Locate every leukocyte (white blood cell).
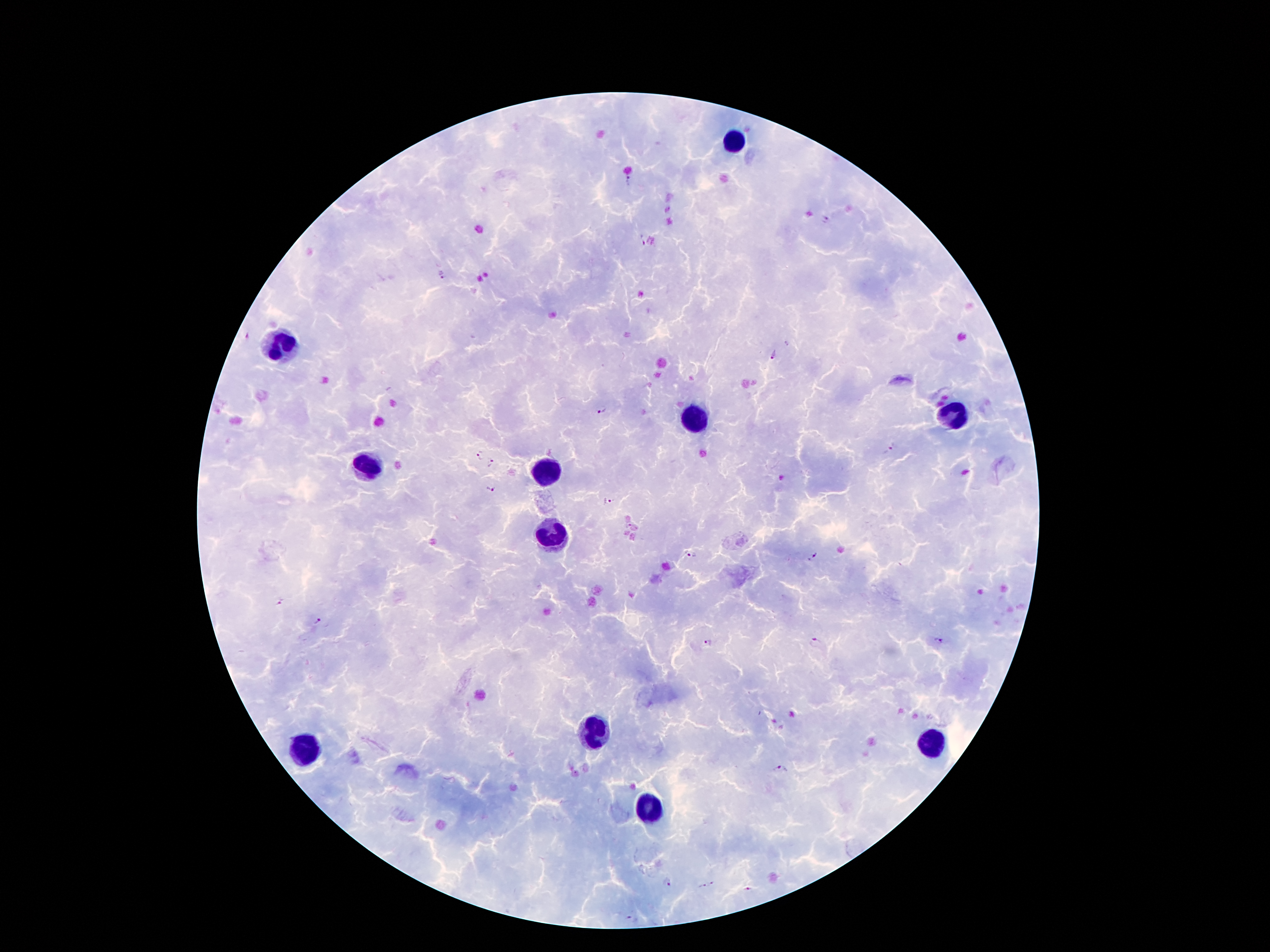

Approximate centers as [x, y] in pixels.
Leukocytes: [734, 141], [282, 345], [952, 415], [695, 418], [370, 468], [545, 472], [552, 533], [593, 733], [927, 744], [302, 749], [647, 810].

Plasmodium parasite locations: [630, 181], [824, 218], [640, 240], [444, 274], [774, 355], [602, 411], [888, 452], [479, 456], [490, 461], [491, 490], [607, 502], [690, 553], [811, 558], [278, 603], [318, 619], [939, 640], [708, 643], [818, 644], [780, 769], [668, 883], [711, 885], [700, 886], [747, 888], [631, 919]. One field from this slide. Image is 1270×952 pixels. Thick blood smear. 100x magnification. Giemsa-stained preparation. Smartphone photograph taken through the microscope eyepiece. Patient malaria status: infected with Plasmodium falciparum.